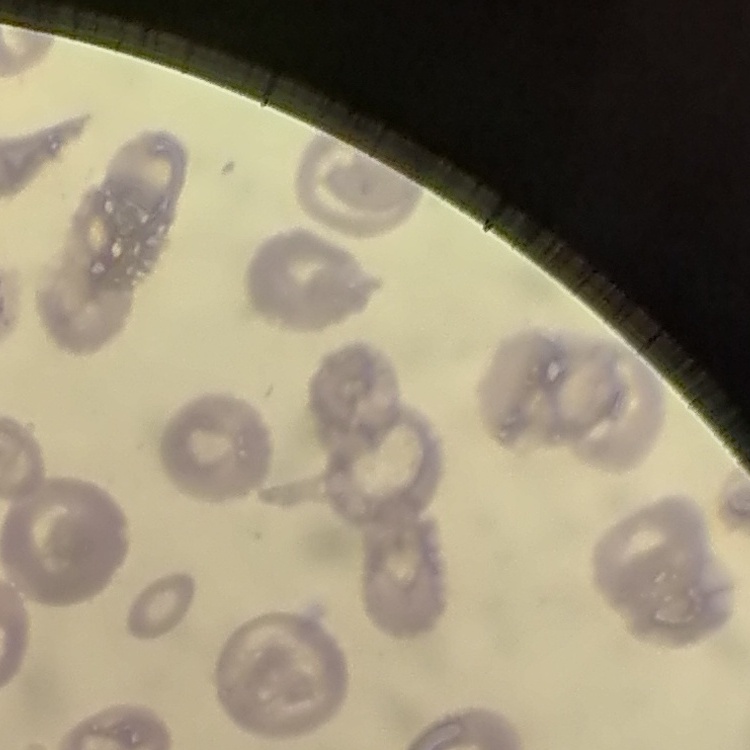

The red blood cells show no rouleaux formation. Field's or Giemsa stain. Square crop of a larger photomicrograph. Thin peripheral smear.